Comment on the morphology of the red blood cells.
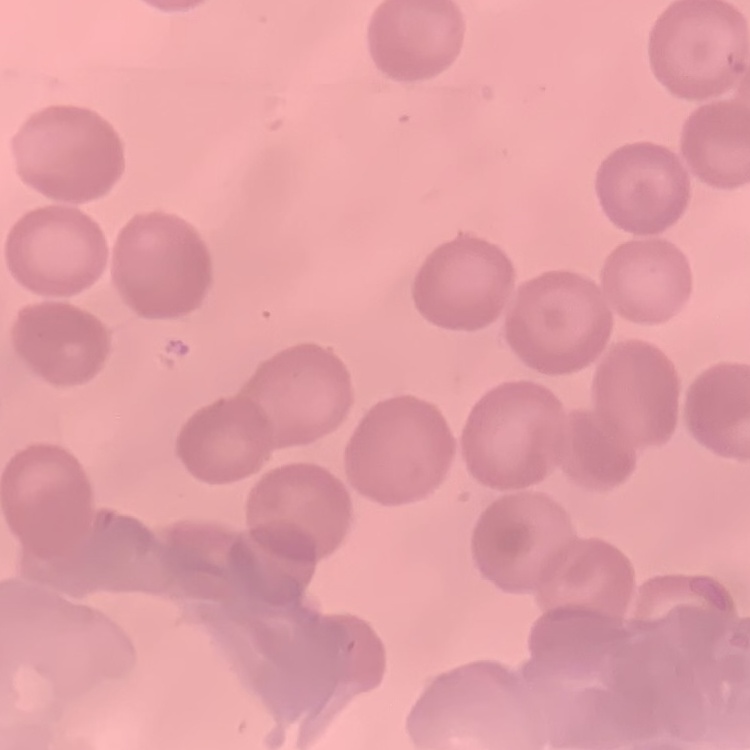

They show no rouleaux formation.

Summary:
  - Image type: one tile cut from a larger photomicrograph
  - Stain: Field's or Giemsa
  - Preparation: thin blood smear